Locate and identify every blood parasite.
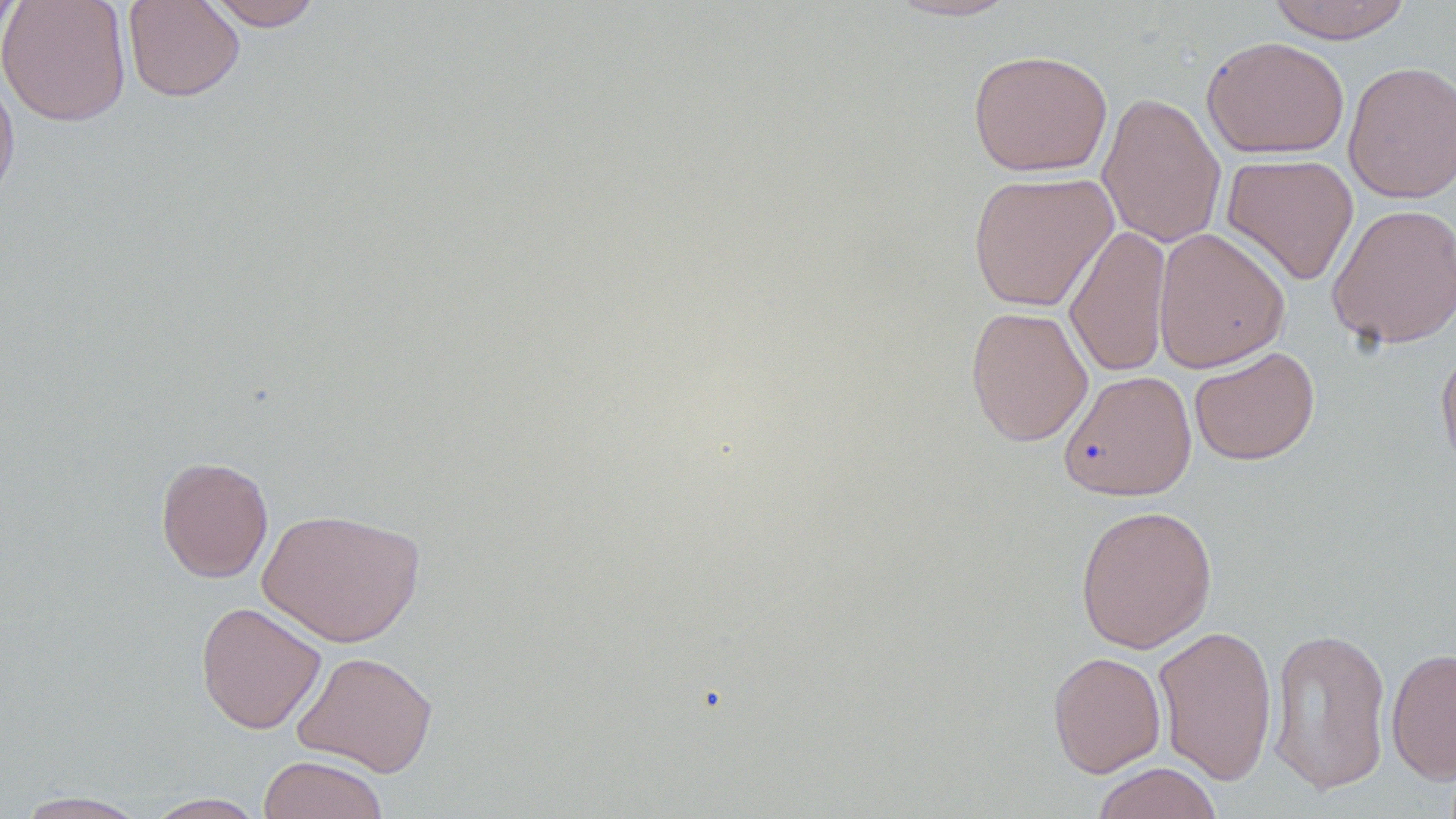

No blood parasites seen.

Approximate bounding boxes as (x1,y1)-(x2,y2) corner pairs in pixels. Uninfected red blood cell locations: (0,0)-(131,126), (0,0)-(21,53), (122,0)-(245,102), (204,0)-(323,31), (884,0)-(1023,22), (1265,0)-(1414,43), (1201,36)-(1350,159), (968,48)-(1113,177), (1343,60)-(1456,204), (0,69)-(20,214), (1096,91)-(1226,249), (1220,153)-(1359,286), (967,171)-(1118,312), (1326,203)-(1456,349), (1064,224)-(1172,379), (1152,227)-(1290,373), (965,305)-(1093,446), (1436,342)-(1456,478), (1188,346)-(1320,466), (1058,369)-(1197,501), (155,456)-(274,583), (1074,504)-(1217,654), (258,507)-(425,647), (195,601)-(326,734), (1152,624)-(1278,785), (1266,626)-(1393,795), (1386,647)-(1456,784), (292,650)-(438,777), (1047,650)-(1166,778), (258,755)-(390,819), (1091,762)-(1224,819), (12,790)-(152,818), (141,792)-(269,818). Slide-level diagnosis: no evidence of blood parasites. Image is 1456×819 pixels. Captured at 1000x magnification. One field of a larger specimen. Light microscopy. Thin blood film. May-Grünwald-Giemsa stain.